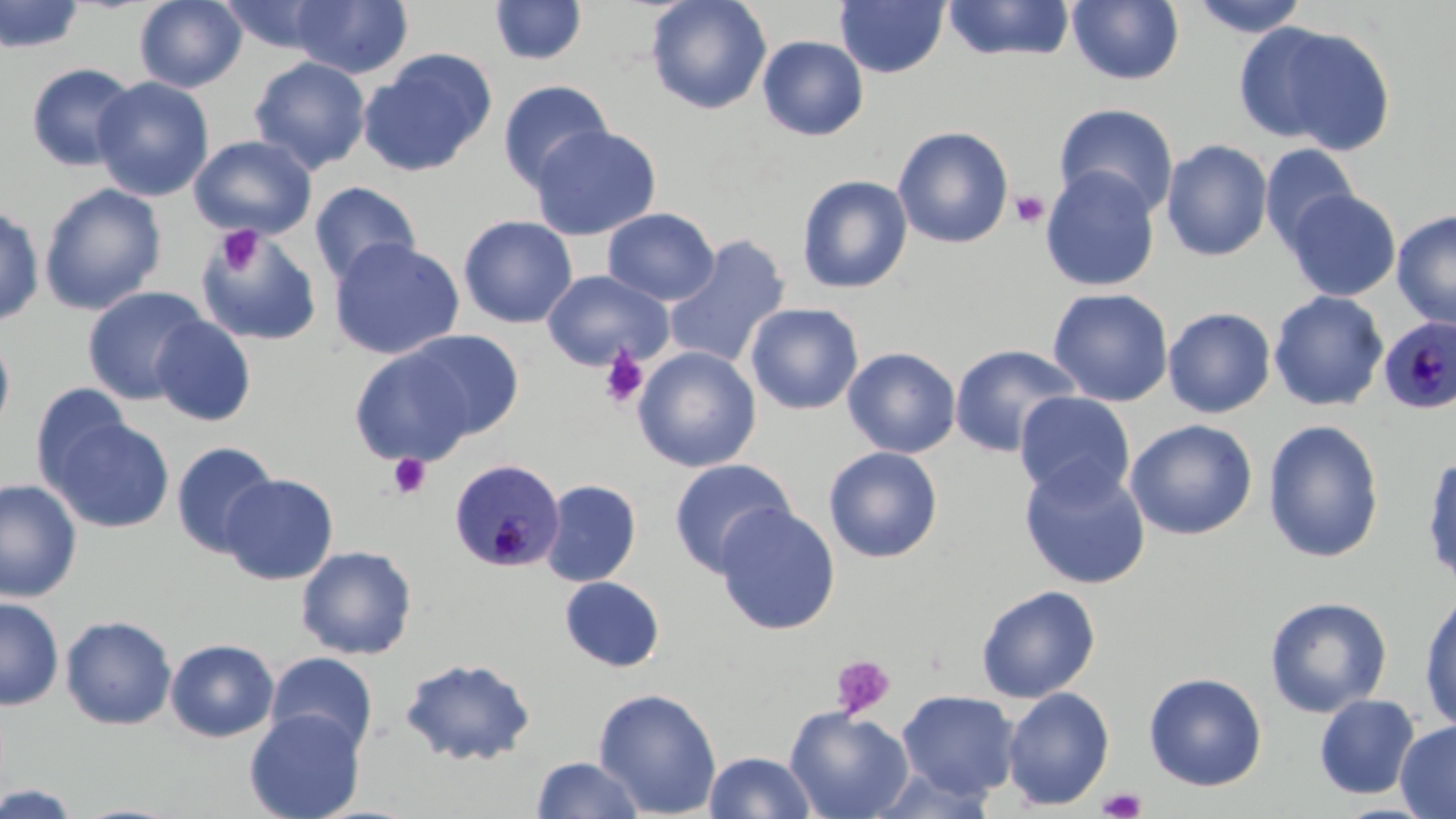
slide-level diagnosis = Plasmodium malariae
preparation = thin blood smear
magnification = 1000x
field of view = one of a larger specimen
stain = May-Grünwald-Giemsa
modality = optical microscopy
uninfected red blood cell locations = approximate bounding boxes as named x1/y1/x2/y2 corners in pixels: (x1=0, y1=0, x2=86, y2=54), (x1=134, y1=0, x2=247, y2=92), (x1=645, y1=0, x2=772, y2=115), (x1=940, y1=0, x2=1076, y2=63), (x1=1067, y1=0, x2=1184, y2=85), (x1=1190, y1=0, x2=1310, y2=37), (x1=217, y1=1, x2=336, y2=55), (x1=291, y1=1, x2=413, y2=80), (x1=489, y1=1, x2=587, y2=65), (x1=835, y1=1, x2=949, y2=78), (x1=1235, y1=20, x2=1396, y2=153), (x1=757, y1=35, x2=868, y2=141), (x1=360, y1=49, x2=497, y2=177), (x1=249, y1=56, x2=371, y2=174), (x1=26, y1=62, x2=139, y2=172), (x1=92, y1=76, x2=214, y2=201), (x1=497, y1=79, x2=613, y2=192), (x1=1053, y1=102, x2=1179, y2=219), (x1=528, y1=124, x2=662, y2=240), (x1=892, y1=125, x2=1014, y2=249), (x1=189, y1=135, x2=317, y2=239), (x1=1161, y1=140, x2=1273, y2=261), (x1=1260, y1=143, x2=1360, y2=252), (x1=1039, y1=167, x2=1160, y2=293), (x1=796, y1=175, x2=913, y2=294), (x1=309, y1=181, x2=421, y2=287), (x1=39, y1=182, x2=167, y2=315), (x1=1284, y1=189, x2=1401, y2=302), (x1=0, y1=206, x2=45, y2=328), (x1=602, y1=207, x2=720, y2=306), (x1=1391, y1=210, x2=1456, y2=329), (x1=458, y1=214, x2=578, y2=328), (x1=196, y1=226, x2=322, y2=346), (x1=663, y1=235, x2=791, y2=370), (x1=329, y1=237, x2=465, y2=360), (x1=542, y1=269, x2=674, y2=371), (x1=82, y1=286, x2=210, y2=406), (x1=1047, y1=287, x2=1173, y2=407), (x1=1268, y1=290, x2=1389, y2=412), (x1=745, y1=303, x2=864, y2=415), (x1=1162, y1=307, x2=1276, y2=418), (x1=151, y1=316, x2=256, y2=427), (x1=401, y1=330, x2=526, y2=442), (x1=0, y1=332, x2=15, y2=439), (x1=348, y1=343, x2=484, y2=467), (x1=949, y1=344, x2=1083, y2=458), (x1=632, y1=346, x2=761, y2=472), (x1=842, y1=347, x2=961, y2=459), (x1=30, y1=382, x2=134, y2=491), (x1=1015, y1=392, x2=1135, y2=504), (x1=1016, y1=399, x2=1256, y2=526), (x1=48, y1=416, x2=174, y2=534), (x1=1124, y1=419, x2=1258, y2=540), (x1=1262, y1=419, x2=1385, y2=564), (x1=170, y1=441, x2=280, y2=559), (x1=823, y1=446, x2=943, y2=563), (x1=1421, y1=452, x2=1456, y2=594), (x1=668, y1=458, x2=796, y2=578), (x1=1019, y1=462, x2=1152, y2=590), (x1=220, y1=473, x2=339, y2=584), (x1=0, y1=479, x2=82, y2=603), (x1=541, y1=479, x2=641, y2=587), (x1=714, y1=503, x2=840, y2=635), (x1=296, y1=545, x2=418, y2=660), (x1=559, y1=576, x2=665, y2=673), (x1=975, y1=585, x2=1101, y2=703), (x1=1419, y1=592, x2=1456, y2=733), (x1=1, y1=596, x2=64, y2=711), (x1=1264, y1=596, x2=1392, y2=718), (x1=59, y1=615, x2=178, y2=731), (x1=165, y1=638, x2=280, y2=743), (x1=264, y1=651, x2=379, y2=756), (x1=399, y1=656, x2=536, y2=766), (x1=1143, y1=672, x2=1268, y2=791), (x1=1002, y1=687, x2=1115, y2=811), (x1=592, y1=688, x2=722, y2=817), (x1=896, y1=689, x2=1020, y2=800), (x1=1314, y1=694, x2=1420, y2=799), (x1=784, y1=706, x2=914, y2=819), (x1=244, y1=708, x2=365, y2=819), (x1=1395, y1=719, x2=1456, y2=818), (x1=704, y1=751, x2=817, y2=818), (x1=531, y1=756, x2=645, y2=819), (x1=1, y1=784, x2=82, y2=818)
platelet locations = approximate bounding boxes as named x1/y1/x2/y2 corners in pixels: (x1=1010, y1=190, x2=1050, y2=228), (x1=215, y1=227, x2=264, y2=276), (x1=599, y1=347, x2=648, y2=408), (x1=388, y1=454, x2=431, y2=498), (x1=830, y1=654, x2=896, y2=720), (x1=1097, y1=787, x2=1147, y2=819)
Plasmodium malariae-infected red blood cell locations = approximate bounding boxes as named x1/y1/x2/y2 corners in pixels: (x1=1379, y1=317, x2=1456, y2=415), (x1=449, y1=458, x2=565, y2=573)
image size = 1456×819 pixels